Locate every Babesia divergens-infected red blood cell.
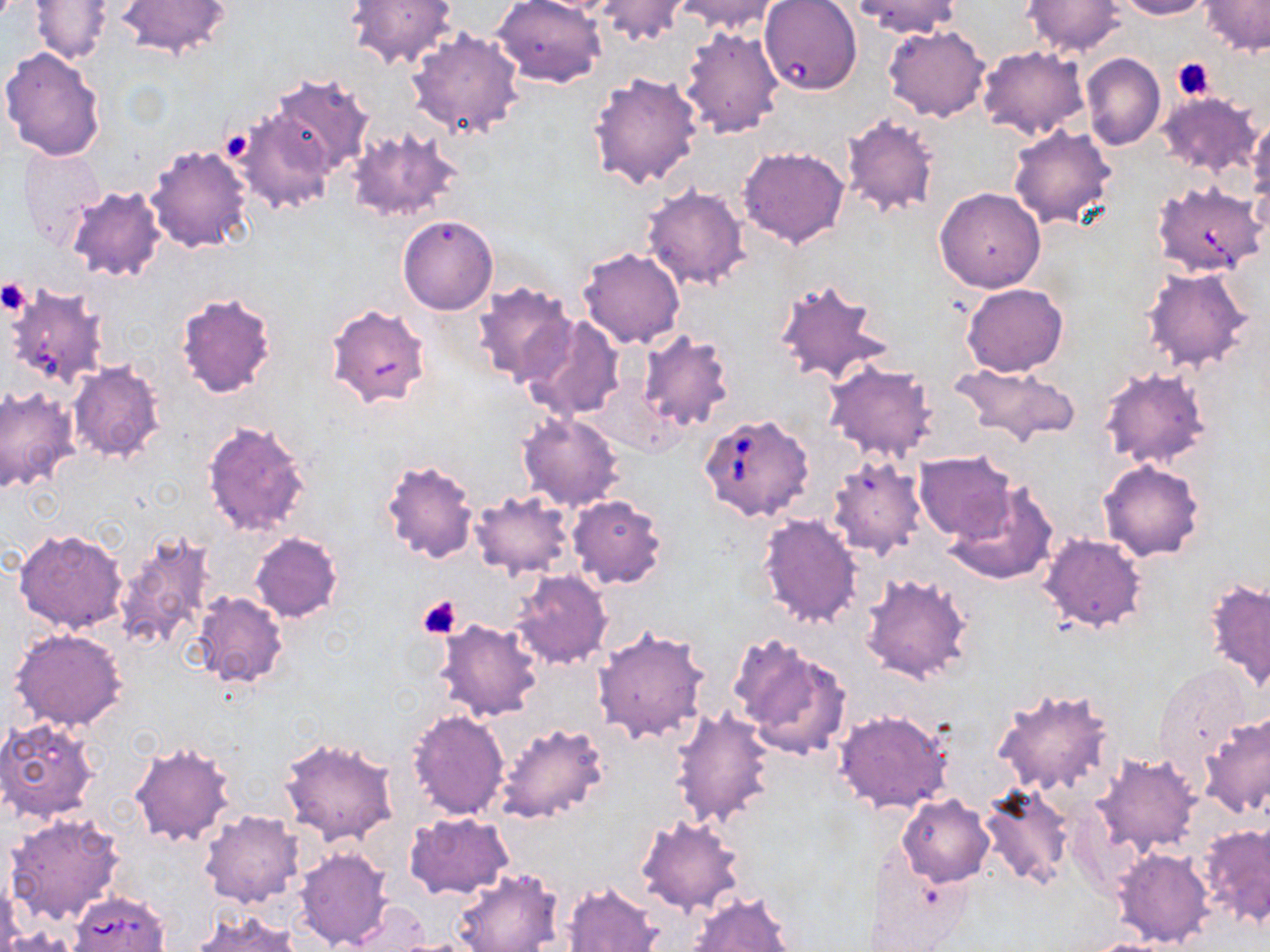

Approximate bounding boxes as [x1, y1, x2, y2] in pixels.
Babesia divergens-infected red blood cells: [1151, 179, 1266, 277], [699, 412, 815, 523], [70, 891, 171, 952].

Uninfected red blood cell locations: [116, 0, 233, 60], [346, 0, 457, 69], [492, 0, 605, 87], [677, 0, 781, 34], [759, 0, 862, 97], [852, 0, 961, 37], [1022, 0, 1126, 56], [1113, 0, 1215, 19], [1200, 0, 1270, 56], [30, 1, 113, 64], [596, 1, 692, 49], [883, 24, 991, 122], [681, 25, 785, 140], [405, 28, 527, 139], [976, 46, 1090, 141], [1, 47, 107, 162], [1081, 53, 1165, 150], [588, 72, 703, 191], [268, 75, 375, 176], [1156, 91, 1263, 177], [233, 105, 338, 213], [841, 111, 943, 220], [1246, 120, 1270, 202], [1008, 124, 1117, 229], [344, 125, 465, 224], [144, 143, 254, 253], [737, 145, 851, 249], [16, 146, 106, 252], [642, 183, 751, 290], [66, 184, 167, 283], [934, 187, 1046, 293], [398, 215, 498, 315], [576, 247, 686, 349], [1141, 267, 1257, 373], [772, 276, 891, 386], [471, 280, 577, 386], [5, 282, 110, 390], [961, 283, 1068, 376], [174, 289, 279, 397], [325, 303, 433, 411], [522, 315, 623, 420], [635, 329, 735, 433], [822, 358, 940, 463], [68, 359, 167, 464], [950, 361, 1081, 450], [1098, 366, 1210, 471], [0, 384, 80, 495], [517, 410, 624, 512], [200, 419, 311, 536], [913, 450, 1016, 542], [826, 454, 928, 561], [380, 457, 479, 564], [1098, 459, 1205, 563], [946, 485, 1058, 586], [468, 491, 576, 580], [566, 494, 669, 589], [756, 511, 863, 629], [14, 528, 129, 634], [112, 529, 217, 657], [249, 531, 343, 623], [1039, 532, 1147, 633], [511, 569, 613, 668], [859, 571, 973, 684], [1204, 580, 1270, 690], [189, 592, 289, 690], [432, 619, 542, 722], [592, 624, 710, 747], [9, 626, 128, 731], [731, 635, 851, 760], [1152, 663, 1251, 775], [992, 685, 1117, 799], [669, 707, 775, 829], [407, 709, 510, 819], [833, 709, 953, 814], [1199, 712, 1270, 819], [0, 716, 103, 824], [494, 720, 609, 823], [277, 736, 399, 846], [129, 739, 237, 848], [1090, 751, 1202, 857], [976, 782, 1076, 891], [897, 793, 995, 886], [5, 811, 126, 926], [199, 811, 304, 909], [404, 813, 515, 899], [634, 814, 747, 916], [1197, 822, 1270, 928], [294, 845, 394, 951], [1112, 847, 1215, 948], [865, 849, 974, 951], [451, 867, 563, 952], [561, 880, 663, 952], [686, 890, 796, 952], [344, 902, 432, 950], [190, 910, 301, 952], [390, 936, 490, 951], [1080, 938, 1183, 952]. Platelet locations: [1172, 58, 1216, 101], [221, 129, 257, 161], [0, 280, 31, 315], [419, 595, 462, 640]. Slide-level diagnosis: Babesia divergens. Single field of view. Thin blood smear. Image is 1270×952 pixels. Captured at 1000x magnification. Light microscopy. May-Grünwald-Giemsa-stained preparation.